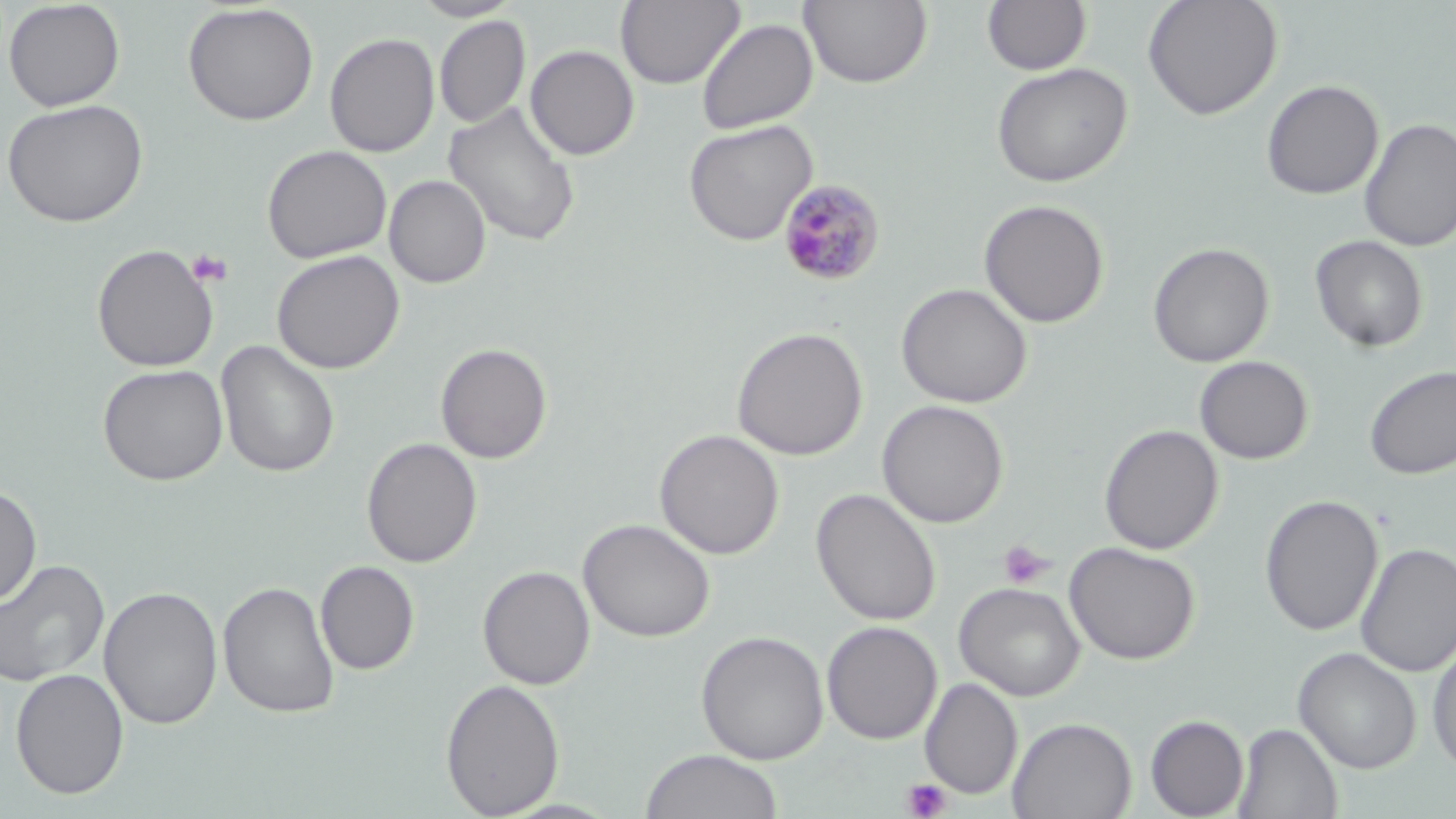
Summary:
  - Coordinate format: approximate bounding boxes as (x1,y1)-(x2,y2) corner pairs in pixels
  - Plasmodium malariae-infected red blood cell locations: (777,178)-(886,288)
  - Uninfected red blood cell locations: (2,0)-(126,112), (410,0)-(523,21), (616,0)-(743,89), (1142,0)-(1283,121), (800,1)-(932,88), (982,1)-(1092,75), (182,3)-(319,126), (434,15)-(531,129), (696,18)-(818,134), (325,32)-(439,158), (525,45)-(639,160), (991,62)-(1132,188), (1261,79)-(1384,199), (2,98)-(149,228), (444,101)-(580,247), (683,119)-(817,246), (1359,119)-(1456,252), (262,145)-(391,264), (384,175)-(490,288), (978,199)-(1109,328), (1310,234)-(1428,352), (1148,242)-(1274,367), (92,244)-(219,372), (271,250)-(404,374), (895,282)-(1033,408), (732,326)-(868,460), (216,340)-(340,478), (435,343)-(553,464), (1194,356)-(1313,464), (97,363)-(228,486), (1364,365)-(1456,479), (877,399)-(1009,528), (1099,424)-(1223,555), (655,429)-(783,559), (361,437)-(482,568), (0,482)-(42,607), (811,487)-(941,626), (1260,494)-(1384,636), (579,518)-(715,642), (1064,541)-(1201,664), (1355,542)-(1456,677), (1,558)-(110,689), (315,560)-(419,675), (478,565)-(595,690), (218,580)-(340,719), (954,581)-(1085,701), (99,585)-(223,730), (821,621)-(942,745), (695,630)-(830,764), (1427,638)-(1456,775), (1293,647)-(1422,773), (10,668)-(129,799), (919,677)-(1023,799), (440,678)-(565,818), (1145,714)-(1249,818), (1008,717)-(1136,819), (1232,722)-(1342,818), (640,749)-(784,819)
  - Platelet locations: (186,248)-(233,288), (997,540)-(1054,589), (902,778)-(952,819)
  - Slide-level diagnosis: Plasmodium malariae
  - Preparation: thin blood film
  - Modality: optical microscopy
  - Field of view: single
  - Image size: 1456×819 pixels
  - Stain: May-Grünwald-Giemsa
  - Magnification: 1000x